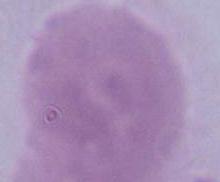
A red blood cell is shown. 1000x magnification. Photomicrograph.